Classify this cell by malaria status.
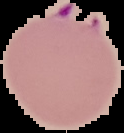
Parasitized.

Summary:
  - Preparation: thin blood smear
  - Image type: segmented cell region on a black background
  - Image size: 124×133 pixels